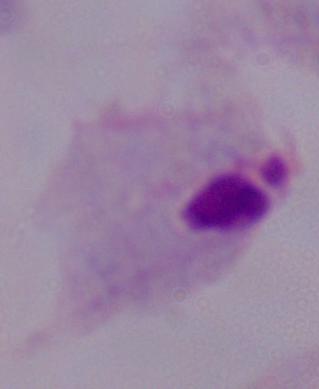
Summary:
  - Identification: trichomonad
  - Magnification: 1000x
  - Modality: photomicrograph